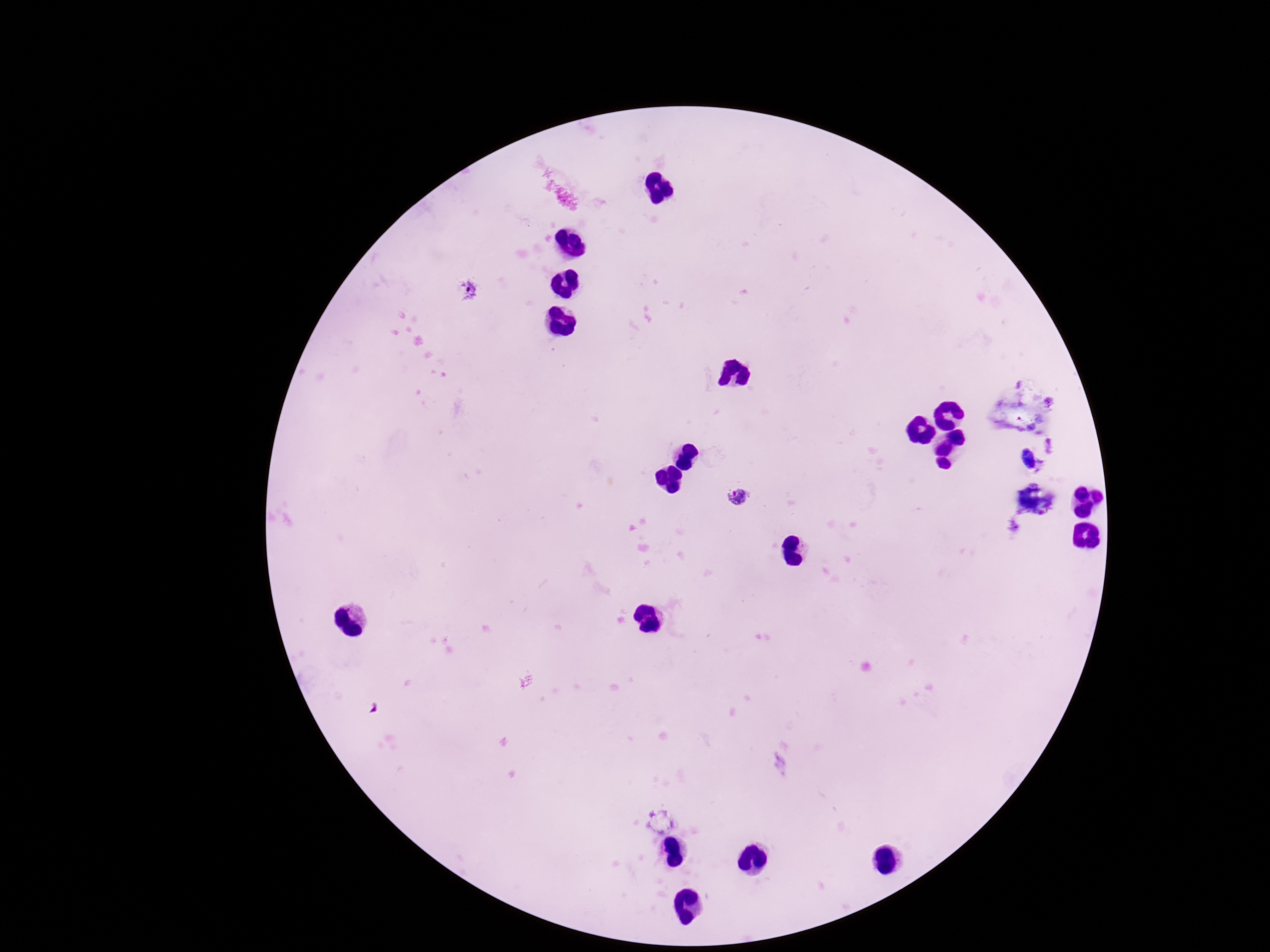

Approximate centers as [x, y] in pixels.
Summary:
  - Plasmodium parasite locations: [466, 292], [737, 497]
  - Field of view: single
  - Capture: smartphone camera through the microscope eyepiece
  - Magnification: 100x
  - Stain: Giemsa
  - Patient malaria status: positive
  - Image size: 1270×952 pixels
  - Preparation: thick blood film